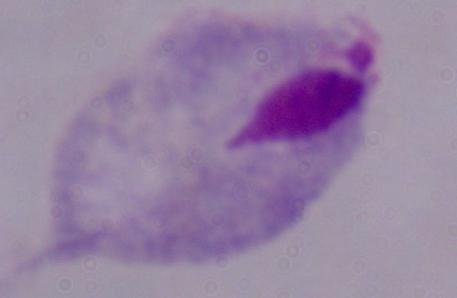
Summary:
  - Identification: trichomonad
  - Modality: photomicrograph
  - Magnification: 1000x